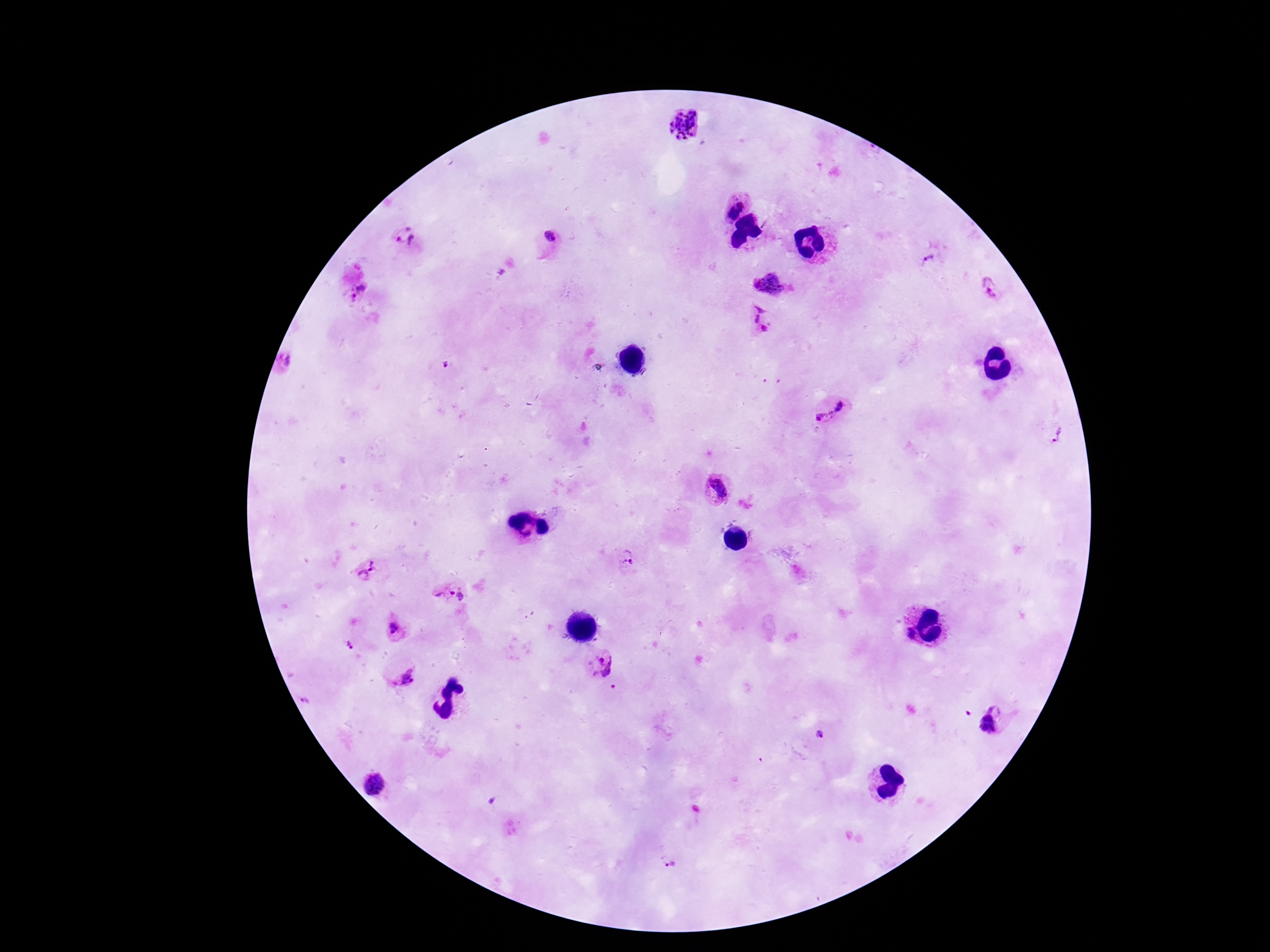
Approximate centers as {x, y} in pixels.
Summary:
  - Plasmodium parasite locations: {685, 126}, {739, 208}, {551, 236}, {406, 238}, {927, 260}, {770, 280}, {990, 288}, {359, 293}, {759, 321}, {286, 364}, {445, 366}, {830, 411}, {1057, 434}, {714, 488}, {629, 557}, {367, 568}, {449, 593}, {394, 630}, {910, 634}, {349, 645}, {599, 664}, {406, 678}, {613, 686}, {967, 713}, {818, 735}, {373, 787}, {491, 802}, {668, 862}
  - Preparation: thick blood film
  - Image size: 1270×952 pixels
  - Stain: Giemsa
  - Capture: smartphone camera through the microscope eyepiece
  - Field of view: one from this slide
  - Magnification: 100x
  - Patient malaria status: positive